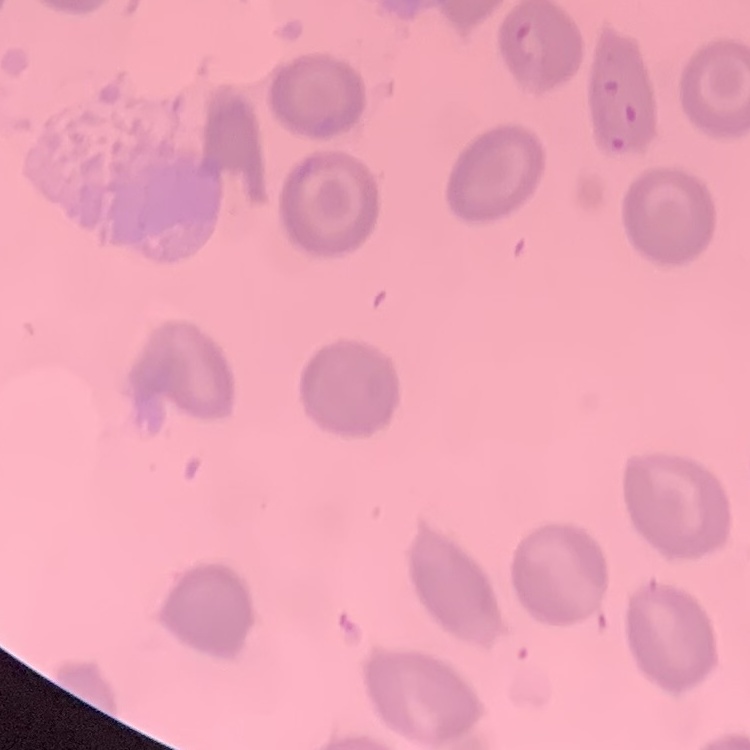
Summary:
  - Erythrocyte morphology: no rouleaux formation
  - Preparation: thin blood film
  - Stain: Field's or Giemsa
  - Image type: one tile cut from a larger photomicrograph